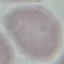

Malaria status: uninfected. Acquired by smartphone through the microscope eyepiece. Giemsa stain. Automatically extracted cell patch, resized to 64 × 64 pixels. Thin smear of blood.